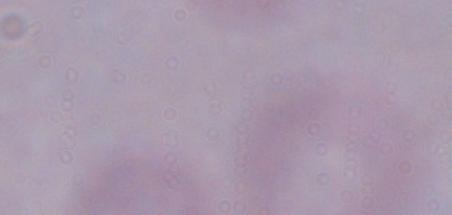

{
  "identification": "trypanosome",
  "modality": "photomicrograph",
  "magnification": "1000x"
}